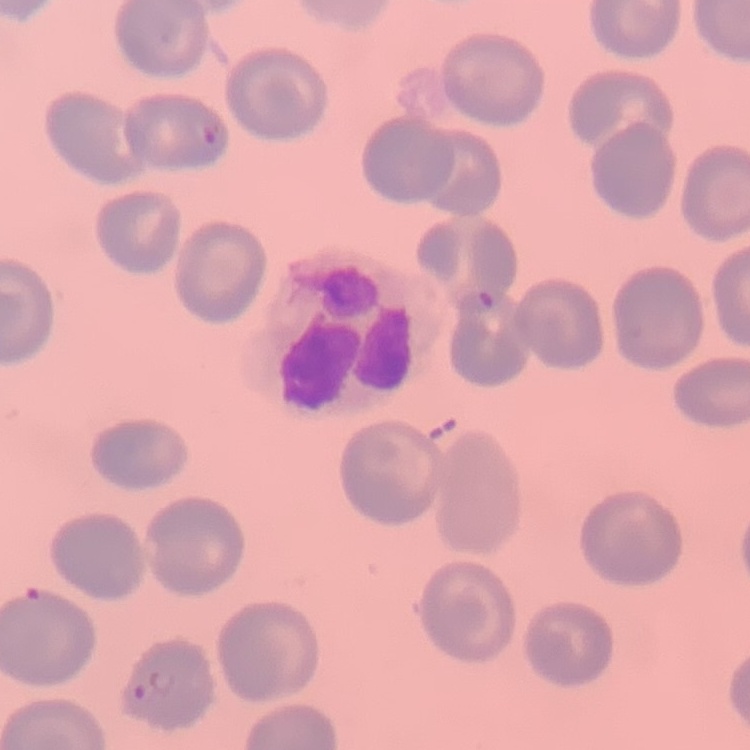

The red blood cells show no rouleaux formation. Stained with either Field's or Giemsa. Thin blood smear. Square crop of a larger photomicrograph.